Assess this cell for malaria.
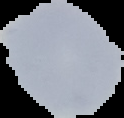

Uninfected.

Image is 124×118 pixels. Segmented cell region on a black background. From a thin blood smear.